State the blood parasite species.
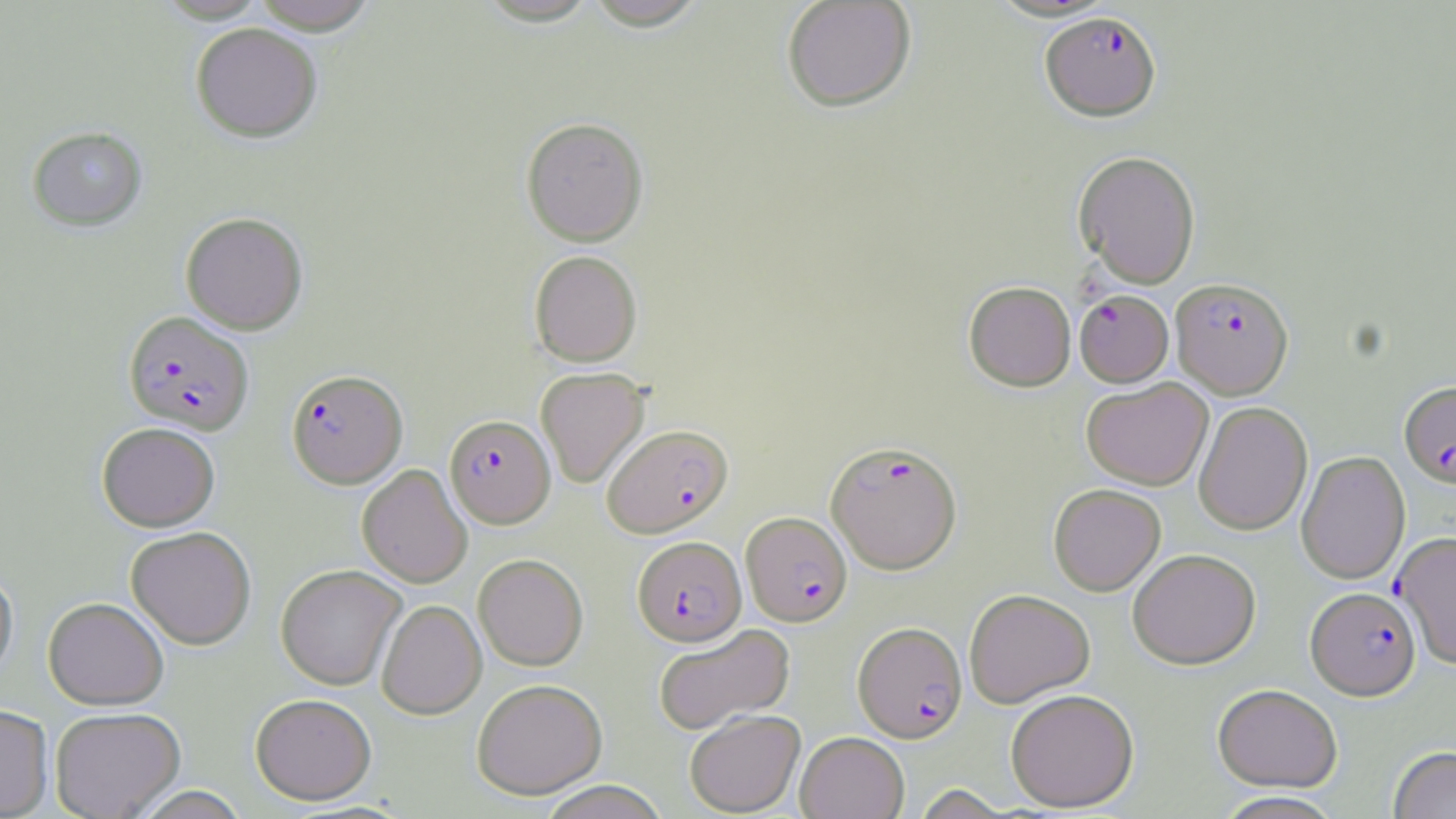
Plasmodium falciparum.

Approximate bounding boxes as (x1,y1)-(x2,y2) corner pairs in pixels. Plasmodium falciparum-infected red blood cell locations: (1041,11)-(1161,122), (1170,277)-(1293,398), (1074,289)-(1173,386), (124,310)-(254,434), (286,368)-(407,488), (1399,381)-(1456,487), (445,414)-(555,528), (601,423)-(733,537), (826,440)-(961,574), (741,512)-(852,626), (1393,533)-(1456,666), (632,536)-(746,646), (1306,586)-(1421,701), (853,622)-(966,742). Uninfected red blood cell locations: (155,0)-(270,22), (249,0)-(380,33), (781,0)-(917,113), (583,1)-(710,31), (190,22)-(323,142), (521,116)-(648,246), (27,126)-(147,231), (1073,150)-(1200,289), (180,211)-(308,334), (529,250)-(642,367), (963,281)-(1076,391), (535,367)-(650,488), (1081,377)-(1213,490), (1193,402)-(1312,535), (96,421)-(220,531), (1296,450)-(1410,584), (356,463)-(472,588), (1049,484)-(1166,595), (126,526)-(256,649), (1127,548)-(1261,669), (473,553)-(588,671), (0,564)-(18,687), (275,564)-(406,690), (963,589)-(1095,707), (43,596)-(169,709), (376,599)-(486,719), (653,623)-(796,735), (471,678)-(607,799), (1213,683)-(1342,791), (1005,689)-(1139,812), (251,693)-(377,805), (0,704)-(54,818), (49,706)-(186,819), (685,709)-(805,817), (795,731)-(909,819), (1388,745)-(1456,819), (537,780)-(671,819), (127,785)-(252,818), (1212,791)-(1346,819). Light microscopy. May-Grünwald-Giemsa-stained preparation. Captured at 1000x magnification. One field of a larger specimen. Image is 1456×819 pixels. Thin blood smear.